Outline each blood parasite and name the species.
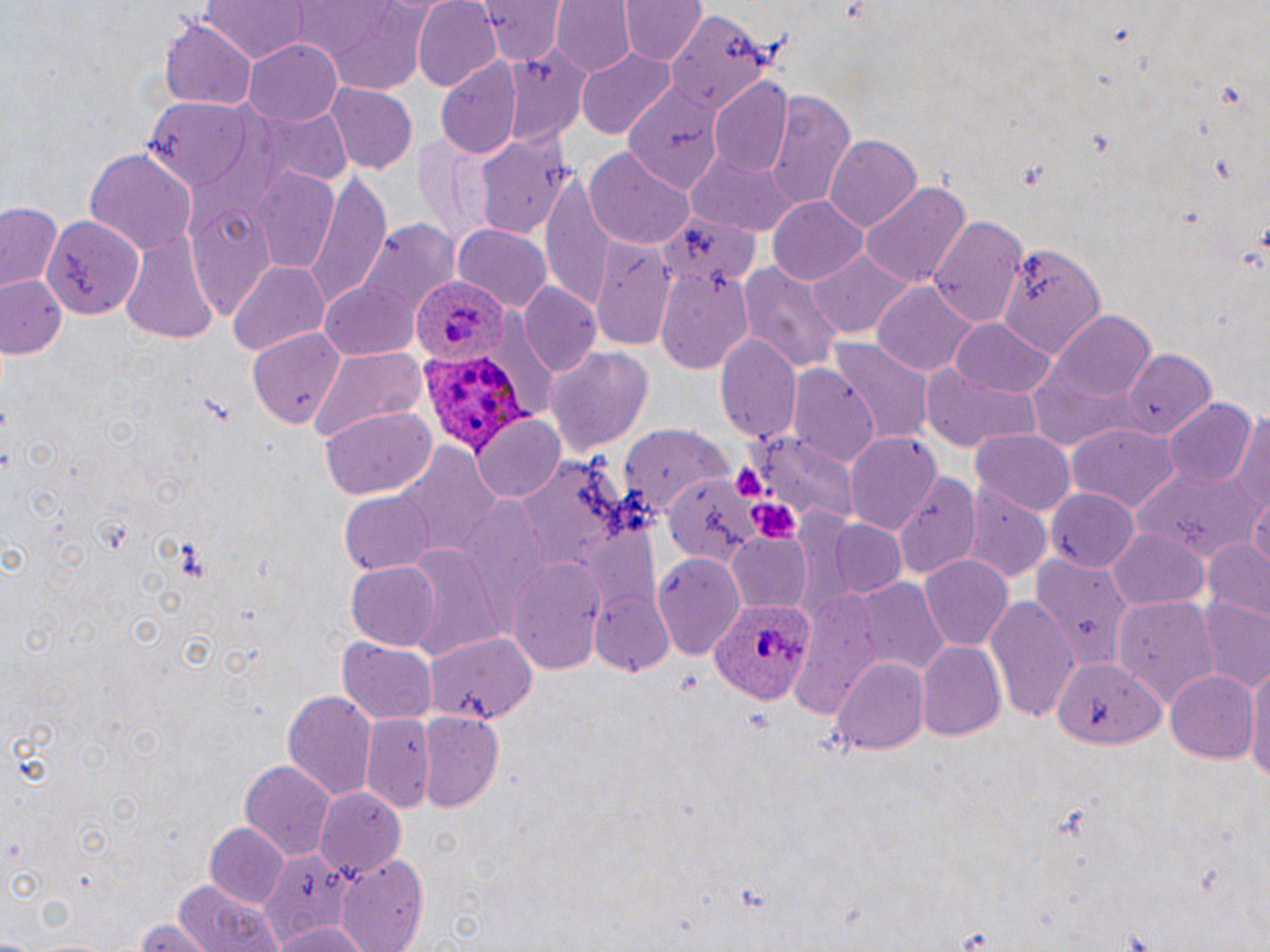
Approximate bounding boxes as named x1/y1/x2/y2 corners in pixels.
Plasmodium ovale-infected red blood cells: (x1=413, y1=274, x2=506, y2=361), (x1=420, y1=352, x2=534, y2=462), (x1=708, y1=598, x2=813, y2=703).
No Plasmodium falciparum, Plasmodium malariae, Plasmodium vivax, Babesia divergens, or Trypanosoma brucei observed.

slide-level diagnosis = Plasmodium ovale
field of view = single
preparation = thin blood film
magnification = 1000x
platelet locations = approximate bounding boxes as named x1/y1/x2/y2 corners in pixels: (x1=730, y1=458, x2=767, y2=500), (x1=749, y1=501, x2=801, y2=540)
uninfected red blood cell locations = approximate bounding boxes as named x1/y1/x2/y2 corners in pixels: (x1=198, y1=0, x2=319, y2=63), (x1=480, y1=0, x2=564, y2=64), (x1=553, y1=0, x2=635, y2=76), (x1=620, y1=0, x2=702, y2=66), (x1=412, y1=1, x2=500, y2=90), (x1=281, y1=2, x2=439, y2=90), (x1=672, y1=11, x2=770, y2=114), (x1=159, y1=19, x2=257, y2=108), (x1=245, y1=38, x2=344, y2=125), (x1=499, y1=43, x2=589, y2=143), (x1=576, y1=47, x2=676, y2=138), (x1=436, y1=56, x2=522, y2=157), (x1=710, y1=78, x2=793, y2=174), (x1=328, y1=85, x2=416, y2=174), (x1=623, y1=88, x2=719, y2=190), (x1=762, y1=89, x2=854, y2=208), (x1=139, y1=94, x2=269, y2=192), (x1=241, y1=105, x2=352, y2=192), (x1=474, y1=126, x2=574, y2=241), (x1=412, y1=132, x2=500, y2=243), (x1=823, y1=134, x2=923, y2=232), (x1=686, y1=145, x2=801, y2=236), (x1=84, y1=147, x2=196, y2=256), (x1=588, y1=148, x2=694, y2=249), (x1=248, y1=169, x2=341, y2=272), (x1=543, y1=172, x2=613, y2=314), (x1=303, y1=174, x2=393, y2=304), (x1=859, y1=181, x2=971, y2=291), (x1=769, y1=196, x2=868, y2=284), (x1=0, y1=201, x2=63, y2=291), (x1=42, y1=214, x2=142, y2=318), (x1=928, y1=214, x2=1029, y2=328), (x1=659, y1=216, x2=753, y2=294), (x1=342, y1=218, x2=463, y2=337), (x1=116, y1=222, x2=220, y2=345), (x1=453, y1=225, x2=554, y2=311), (x1=591, y1=238, x2=672, y2=351), (x1=995, y1=241, x2=1103, y2=360), (x1=807, y1=250, x2=914, y2=340), (x1=227, y1=259, x2=331, y2=358), (x1=739, y1=263, x2=844, y2=373), (x1=655, y1=264, x2=755, y2=370), (x1=3, y1=276, x2=66, y2=357), (x1=321, y1=282, x2=424, y2=359), (x1=521, y1=283, x2=602, y2=376), (x1=873, y1=284, x2=979, y2=379), (x1=1049, y1=310, x2=1159, y2=406), (x1=951, y1=319, x2=1057, y2=398), (x1=250, y1=326, x2=344, y2=428), (x1=715, y1=332, x2=800, y2=445), (x1=828, y1=340, x2=933, y2=443), (x1=545, y1=345, x2=657, y2=455), (x1=308, y1=346, x2=430, y2=444), (x1=1118, y1=348, x2=1219, y2=436), (x1=918, y1=362, x2=1039, y2=452), (x1=789, y1=367, x2=880, y2=469), (x1=1165, y1=398, x2=1258, y2=488), (x1=321, y1=409, x2=435, y2=499), (x1=1230, y1=412, x2=1269, y2=522), (x1=471, y1=415, x2=564, y2=504), (x1=1068, y1=423, x2=1178, y2=514), (x1=620, y1=425, x2=734, y2=514), (x1=971, y1=429, x2=1075, y2=514), (x1=752, y1=431, x2=858, y2=528), (x1=845, y1=431, x2=942, y2=536), (x1=390, y1=444, x2=496, y2=564), (x1=515, y1=457, x2=625, y2=572), (x1=1127, y1=460, x2=1265, y2=562), (x1=892, y1=470, x2=983, y2=579), (x1=662, y1=473, x2=757, y2=566), (x1=962, y1=480, x2=1051, y2=581), (x1=1045, y1=487, x2=1138, y2=571), (x1=337, y1=490, x2=439, y2=577), (x1=1251, y1=495, x2=1269, y2=574), (x1=829, y1=518, x2=908, y2=596), (x1=1108, y1=528, x2=1209, y2=610), (x1=725, y1=531, x2=812, y2=612), (x1=1204, y1=539, x2=1270, y2=620), (x1=654, y1=552, x2=746, y2=657), (x1=1032, y1=553, x2=1131, y2=669), (x1=919, y1=555, x2=1012, y2=649), (x1=507, y1=557, x2=607, y2=672), (x1=345, y1=559, x2=442, y2=650), (x1=851, y1=578, x2=951, y2=673), (x1=588, y1=585, x2=675, y2=679), (x1=802, y1=586, x2=883, y2=719), (x1=985, y1=595, x2=1081, y2=722), (x1=1114, y1=595, x2=1217, y2=709), (x1=1196, y1=599, x2=1270, y2=691), (x1=426, y1=632, x2=536, y2=723), (x1=337, y1=639, x2=437, y2=726), (x1=916, y1=643, x2=1005, y2=743), (x1=831, y1=655, x2=930, y2=756), (x1=1053, y1=659, x2=1161, y2=752), (x1=1247, y1=665, x2=1270, y2=781), (x1=1164, y1=669, x2=1259, y2=764), (x1=283, y1=689, x2=376, y2=801), (x1=417, y1=712, x2=503, y2=810), (x1=363, y1=713, x2=436, y2=810), (x1=240, y1=761, x2=335, y2=859), (x1=313, y1=787, x2=407, y2=876), (x1=203, y1=823, x2=291, y2=909), (x1=260, y1=849, x2=354, y2=946), (x1=336, y1=859, x2=433, y2=952), (x1=174, y1=880, x2=283, y2=952), (x1=132, y1=918, x2=209, y2=951), (x1=268, y1=922, x2=374, y2=952)
image size = 1270×952 pixels
stain = May-Grünwald-Giemsa
modality = optical microscopy